Point out each malaria parasite and each leukocyte.
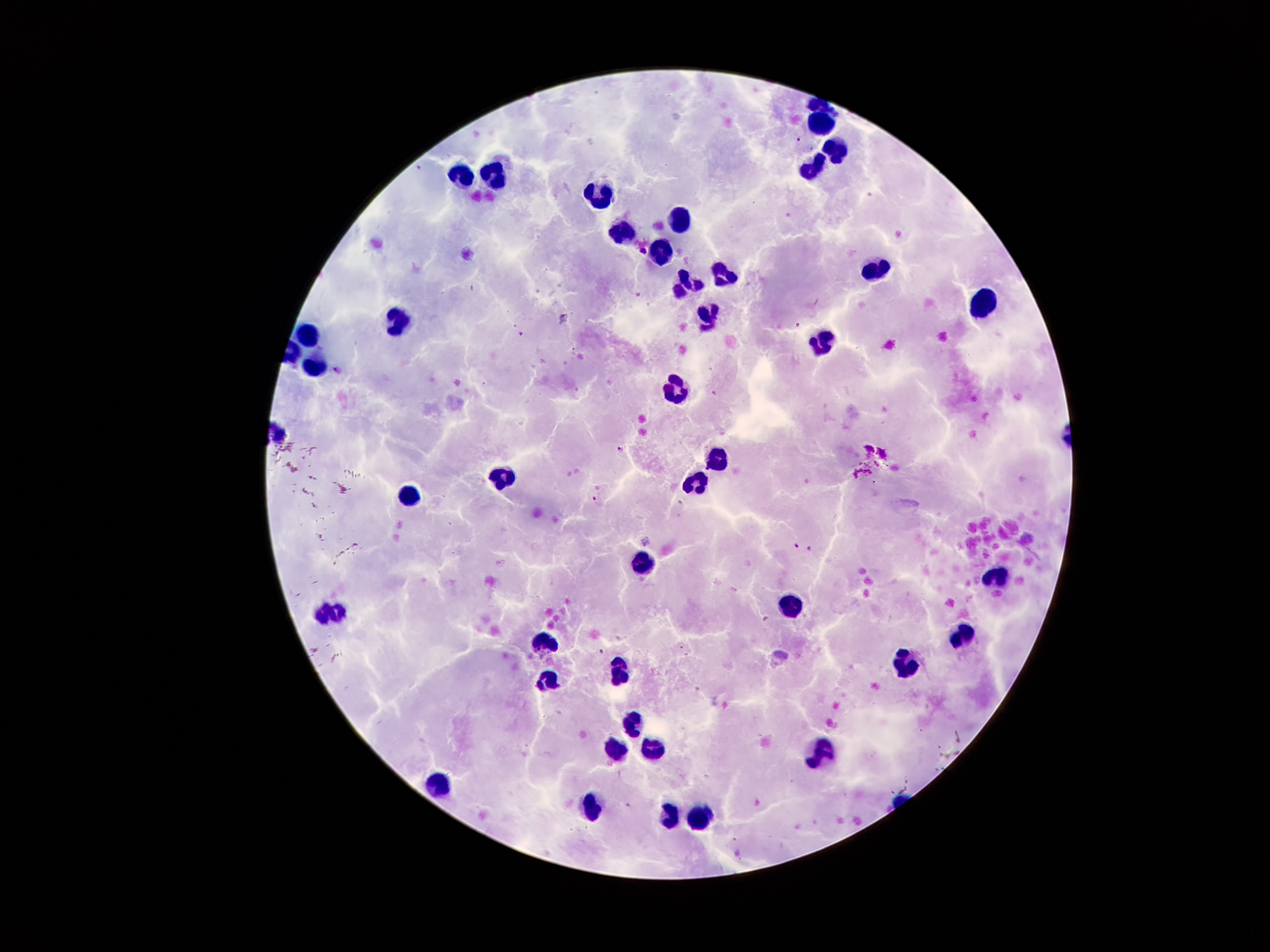

Approximate centers as (x, y) in pixels.
Malaria parasites: (798, 139), (643, 249), (638, 295), (798, 326), (521, 334), (337, 370), (621, 448), (596, 500), (795, 546), (811, 549).
Leukocytes: (822, 121), (832, 146), (813, 167), (462, 176), (494, 178), (602, 196), (680, 220), (622, 235), (663, 253), (874, 268), (724, 278), (692, 285), (982, 301), (705, 320), (399, 322), (308, 337), (824, 337), (319, 360), (682, 390), (720, 459), (501, 476), (699, 480), (406, 497), (643, 562), (998, 572), (790, 609), (332, 615), (963, 631), (544, 638), (904, 665), (618, 669), (548, 683), (631, 725), (654, 748), (822, 751), (612, 752), (444, 784), (590, 808), (671, 818), (698, 818).

{
  "image_size": "1270×952 pixels",
  "capture": "smartphone through the microscope eyepiece",
  "magnification": "100x",
  "preparation": "thick blood film",
  "patient_malaria_status": "positive for Plasmodium falciparum",
  "stain": "Giemsa",
  "field_of_view": "single"
}